Report the malaria status of this cell.
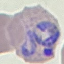
It is parasitized.

Photographed with a smartphone camera at the microscope eyepiece. Cell patch, automatically extracted from a larger field of view and resized to 64 × 64 pixels. Giemsa stain. Thin smear of blood.